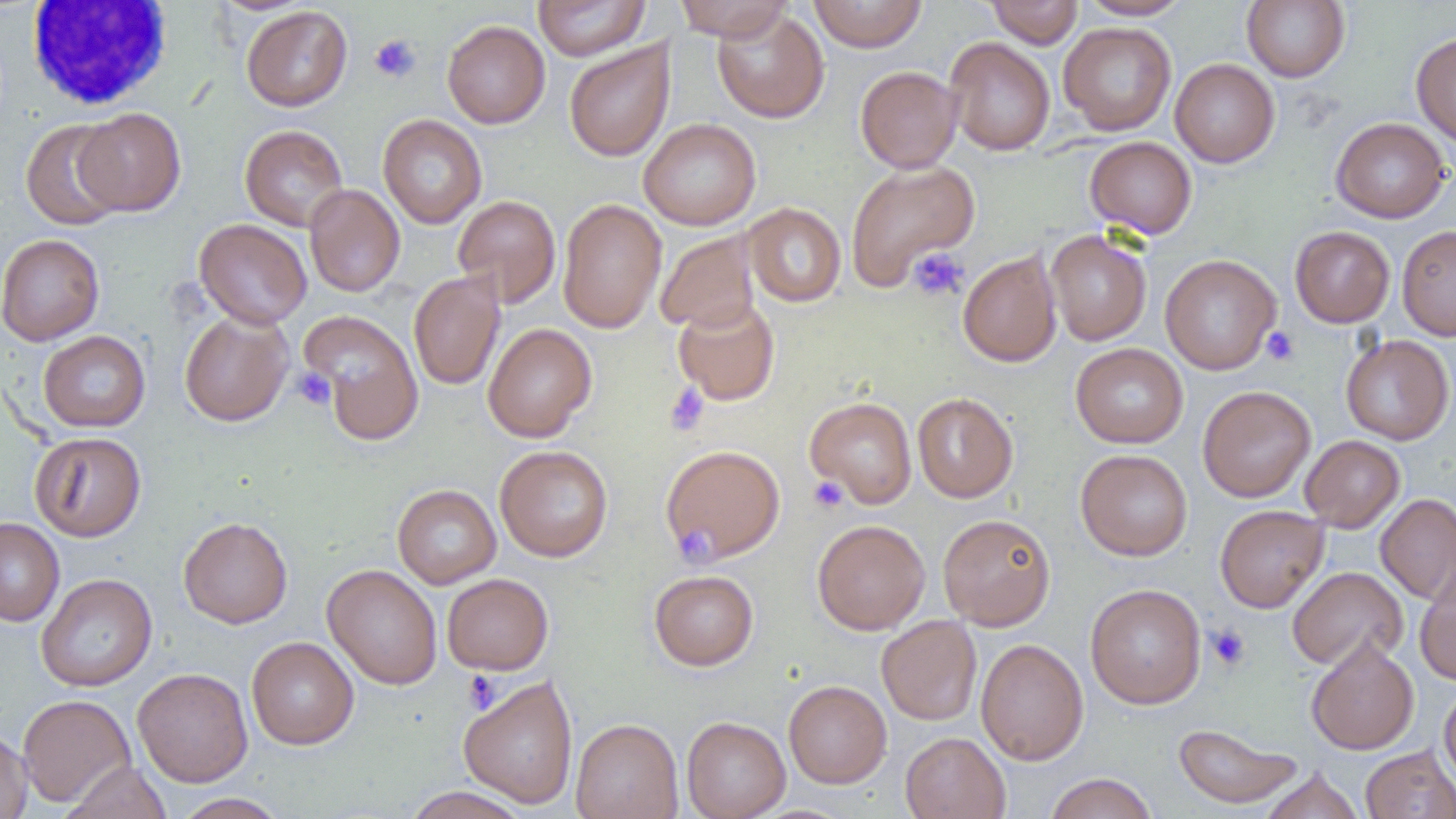
{
  "slide_level_diagnosis": "negative for blood parasites",
  "uninfected_red_blood_cell_locations": "approximate bounding boxes as (x1,y1)-(x2,y2) corner pairs in pixels: (533,0)-(650,60), (673,0)-(794,41), (808,0)-(927,52), (985,0)-(1083,48), (1076,0)-(1192,20), (1242,1)-(1350,82), (241,5)-(353,111), (711,7)-(829,124), (442,20)-(550,128), (1058,22)-(1177,135), (1411,32)-(1456,148), (944,37)-(1055,155), (564,39)-(675,162), (1170,58)-(1280,167), (855,65)-(963,173), (75,108)-(186,216), (377,114)-(487,228), (1331,117)-(1450,222), (638,118)-(761,230), (20,119)-(127,230), (239,124)-(349,232), (1084,136)-(1197,239), (845,159)-(980,291), (304,184)-(405,297), (453,195)-(561,306), (557,199)-(667,334), (743,203)-(846,307), (194,218)-(312,329), (1397,225)-(1456,340), (1290,226)-(1395,327), (654,229)-(761,334), (1045,229)-(1152,345), (0,233)-(105,346), (957,248)-(1063,368), (1160,254)-(1281,374), (408,270)-(506,391), (673,298)-(780,405), (178,310)-(294,427), (301,310)-(426,446), (483,322)-(597,442), (38,330)-(150,432), (1341,334)-(1454,445), (1070,343)-(1188,448), (1198,385)-(1315,502), (912,392)-(1018,502), (805,396)-(917,508), (30,431)-(146,542), (1300,435)-(1405,531), (660,444)-(785,566), (495,445)-(613,562), (1076,449)-(1192,561), (392,484)-(501,589), (1375,493)-(1456,604), (1215,505)-(1328,613), (938,513)-(1056,630), (178,516)-(293,628), (0,518)-(65,626), (812,519)-(930,635), (322,564)-(443,689), (1287,566)-(1408,671), (1415,566)-(1456,686), (649,570)-(759,670), (36,573)-(157,691), (442,573)-(553,674), (1085,583)-(1206,708), (876,615)-(982,726), (246,636)-(359,750), (1306,637)-(1419,754), (975,638)-(1089,765), (132,667)-(253,787), (459,675)-(578,808), (783,680)-(892,788), (1439,682)-(1456,788), (17,694)-(136,807), (681,716)-(791,819), (571,718)-(683,819), (1172,722)-(1304,809), (0,726)-(32,819), (900,731)-(1010,819), (1360,745)-(1456,819), (65,761)-(171,818), (1259,766)-(1364,818), (1044,772)-(1158,819), (402,786)-(531,819), (171,793)-(289,819)",
  "modality": "light microscopy",
  "field_of_view": "one of a larger specimen",
  "platelet_locations": "approximate bounding boxes as (x1,y1)-(x2,y2) corner pairs in pixels: (369,33)-(422,83), (908,247)-(969,301), (1261,327)-(1300,366), (292,367)-(336,410), (664,384)-(710,436), (808,476)-(849,513), (678,528)-(727,564), (1206,624)-(1250,670), (463,670)-(502,714)",
  "magnification": "1000x",
  "preparation": "thin blood smear",
  "white_blood_cell_locations": "approximate bounding boxes as (x1,y1)-(x2,y2) corner pairs in pixels: (26,1)-(174,111)",
  "image_size": "1456×819 pixels"
}